Assess this cell for malaria.
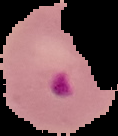

Parasitized.

{
  "image_type": "segmented cell region with the area outside set to black",
  "image_size": "118×136 pixels",
  "preparation": "thin blood film"
}